Assess this cell for malaria.
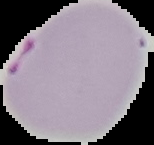
Parasitized.

Summary:
  - Image size: 154×145 pixels
  - Preparation: thin blood film
  - Image type: segmented cell region with the area outside set to black